Give the position of every leukocyte visible.
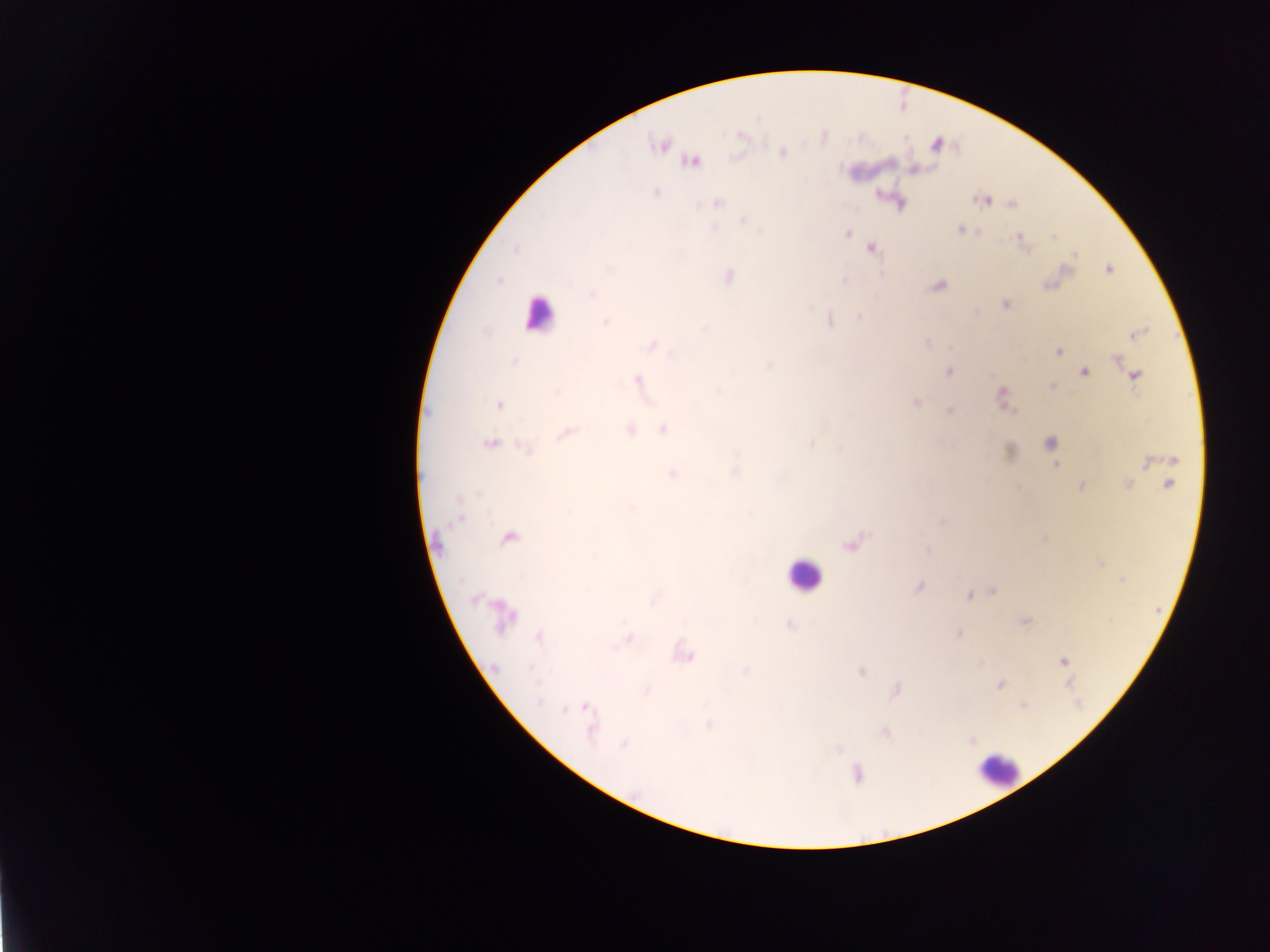
Approximate centers as (x, y) in pixels.
Leukocytes: (538, 313), (804, 576), (997, 768).

{
  "country": "Ghana",
  "preparation": "thick blood film",
  "field_of_view": "single",
  "image_size": "1270×952 pixels",
  "capture": "mobile-phone photograph through a microscope",
  "malaria_parasite_locations": "approximate centers as (x, y) in pixels: (661, 145), (781, 152), (692, 161), (654, 192), (878, 193), (982, 199), (717, 203), (899, 203), (1010, 204), (742, 219), (713, 228), (960, 230), (845, 233), (1053, 235), (1020, 237), (870, 247), (1074, 254), (1108, 269), (881, 274), (727, 276), (497, 280), (843, 281), (937, 286), (591, 293), (1004, 304), (860, 316), (829, 319), (605, 322), (1136, 333), (651, 345), (1057, 351), (1116, 358), (512, 361), (1084, 371), (948, 372), (1134, 375), (637, 380), (1051, 387), (1001, 397), (915, 403), (498, 405), (950, 410), (663, 429), (628, 430), (566, 433), (489, 442), (1050, 442), (811, 444), (525, 446), (1147, 462), (1056, 464), (734, 471), (671, 473), (1128, 483), (1169, 483), (1082, 486), (1018, 487), (459, 517), (941, 521), (508, 536), (851, 542), (927, 550), (1122, 580), (918, 587), (992, 592), (969, 596), (501, 615), (1026, 620), (789, 625), (958, 634), (539, 637), (628, 639), (683, 654), (1062, 661), (860, 671), (1000, 684), (895, 690), (1022, 704), (585, 707), (566, 708), (708, 725), (590, 727), (885, 733), (970, 739), (623, 744), (838, 749), (856, 773)"
}